Outline each Plasmodium ovale-infected red blood cell.
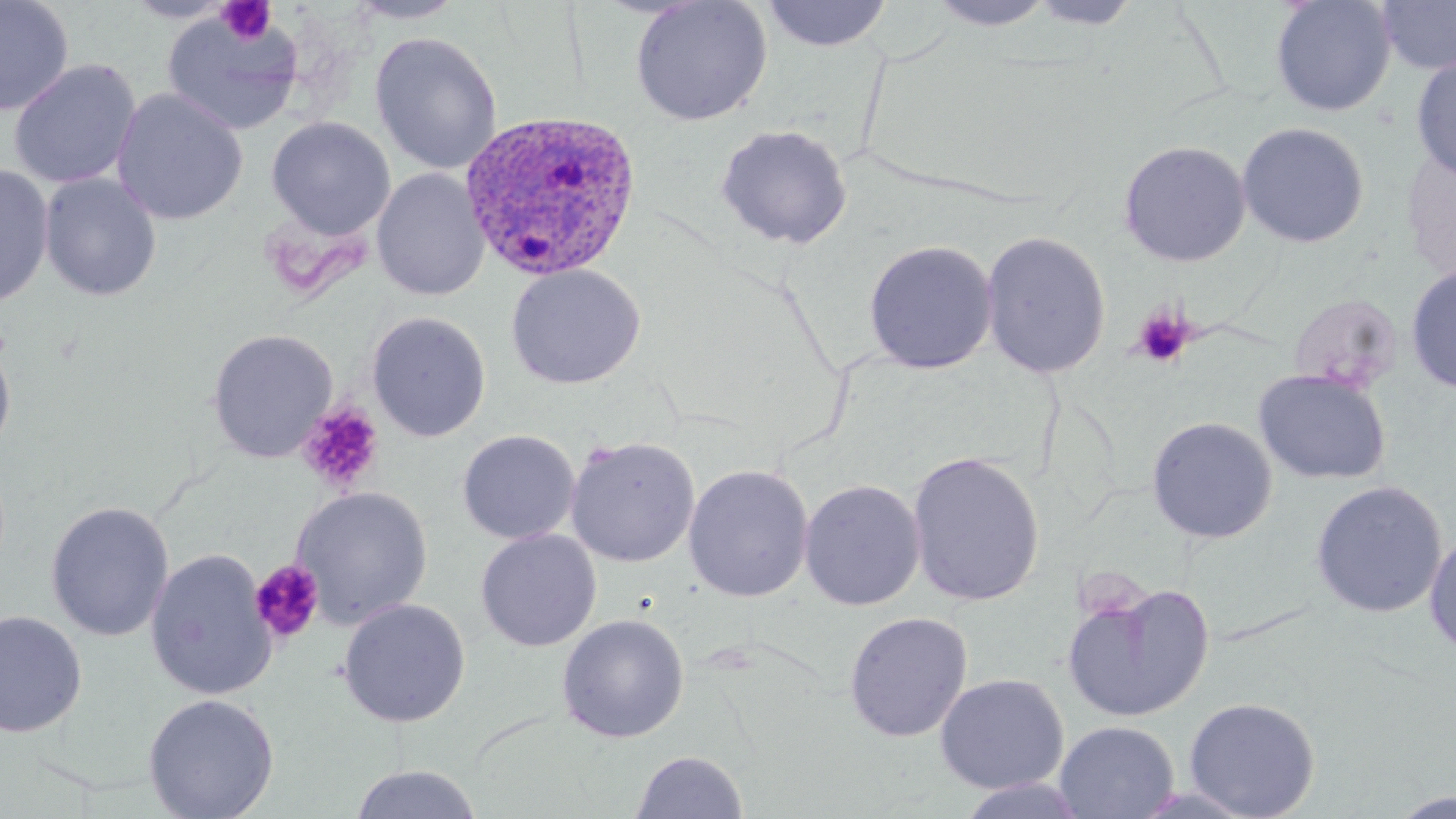

Approximate bounding boxes as (x1, y1, x2, y2) in pixels.
Plasmodium ovale-infected red blood cells: (460, 109, 643, 283).

Platelet locations: (216, 2, 277, 45), (1132, 307, 1194, 368), (297, 401, 384, 493), (249, 560, 324, 644). Uninfected red blood cell locations: (0, 0, 74, 116), (120, 0, 239, 23), (344, 0, 468, 25), (927, 0, 1057, 30), (1026, 0, 1146, 30), (1270, 0, 1397, 117), (1376, 0, 1456, 76), (630, 1, 773, 126), (760, 1, 893, 52), (161, 11, 303, 137), (370, 32, 503, 175), (1411, 55, 1456, 181), (8, 59, 142, 189), (111, 88, 248, 225), (266, 117, 395, 238), (1236, 121, 1370, 248), (715, 124, 852, 248), (1118, 139, 1252, 267), (1401, 147, 1455, 281), (0, 163, 55, 308), (372, 169, 489, 301), (39, 172, 162, 302), (979, 229, 1111, 379), (862, 239, 998, 375), (506, 263, 645, 390), (1405, 264, 1456, 394), (367, 312, 491, 441), (207, 329, 338, 462), (0, 340, 16, 460), (1254, 368, 1392, 485), (1147, 416, 1278, 543), (457, 429, 580, 544), (565, 436, 701, 567), (907, 450, 1045, 607), (683, 464, 814, 602), (798, 478, 926, 611), (1311, 481, 1448, 618), (292, 487, 433, 628), (46, 500, 175, 641), (476, 529, 601, 652), (1424, 530, 1456, 659), (145, 549, 276, 701), (1061, 580, 1215, 723), (338, 598, 470, 727), (0, 610, 87, 738), (843, 611, 973, 742), (556, 613, 690, 743), (934, 673, 1069, 794), (143, 693, 279, 819), (1183, 696, 1320, 818), (1055, 720, 1179, 818), (630, 750, 749, 818), (350, 763, 483, 819), (956, 777, 1091, 818), (1128, 783, 1262, 817), (1388, 791, 1456, 818). Slide-level diagnosis: Plasmodium ovale. Captured at 1000x magnification. Light microscopy. Image is 1456×819 pixels. May-Grünwald-Giemsa-stained preparation. Thin blood film. Single field of view.